Point out each Plasmodium parasite.
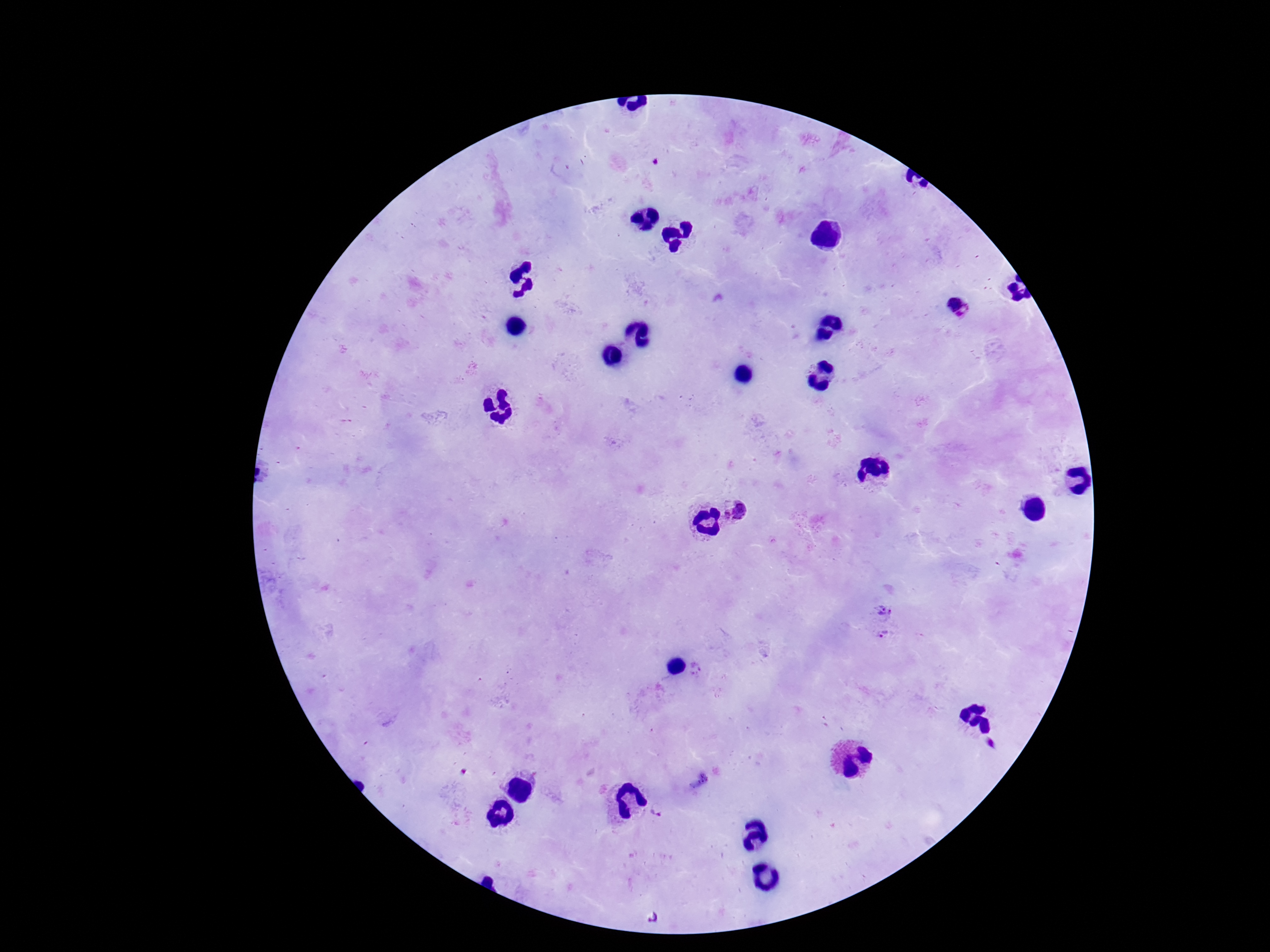
Approximate centers as {x, y} in pixels.
Plasmodium parasites: {745, 510}, {878, 620}, {656, 809}.

Summary:
  - Stain: Giemsa
  - Patient malaria status: positive
  - Field of view: one from this slide
  - Magnification: 100x
  - Image size: 1270×952 pixels
  - Capture: smartphone camera through the microscope eyepiece
  - Preparation: thick blood film